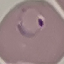
malaria status = parasitized
preparation = thin blood film
capture = smartphone through the microscope eyepiece
image type = automatically extracted cell patch, resized to 64 × 64 pixels
stain = Giemsa